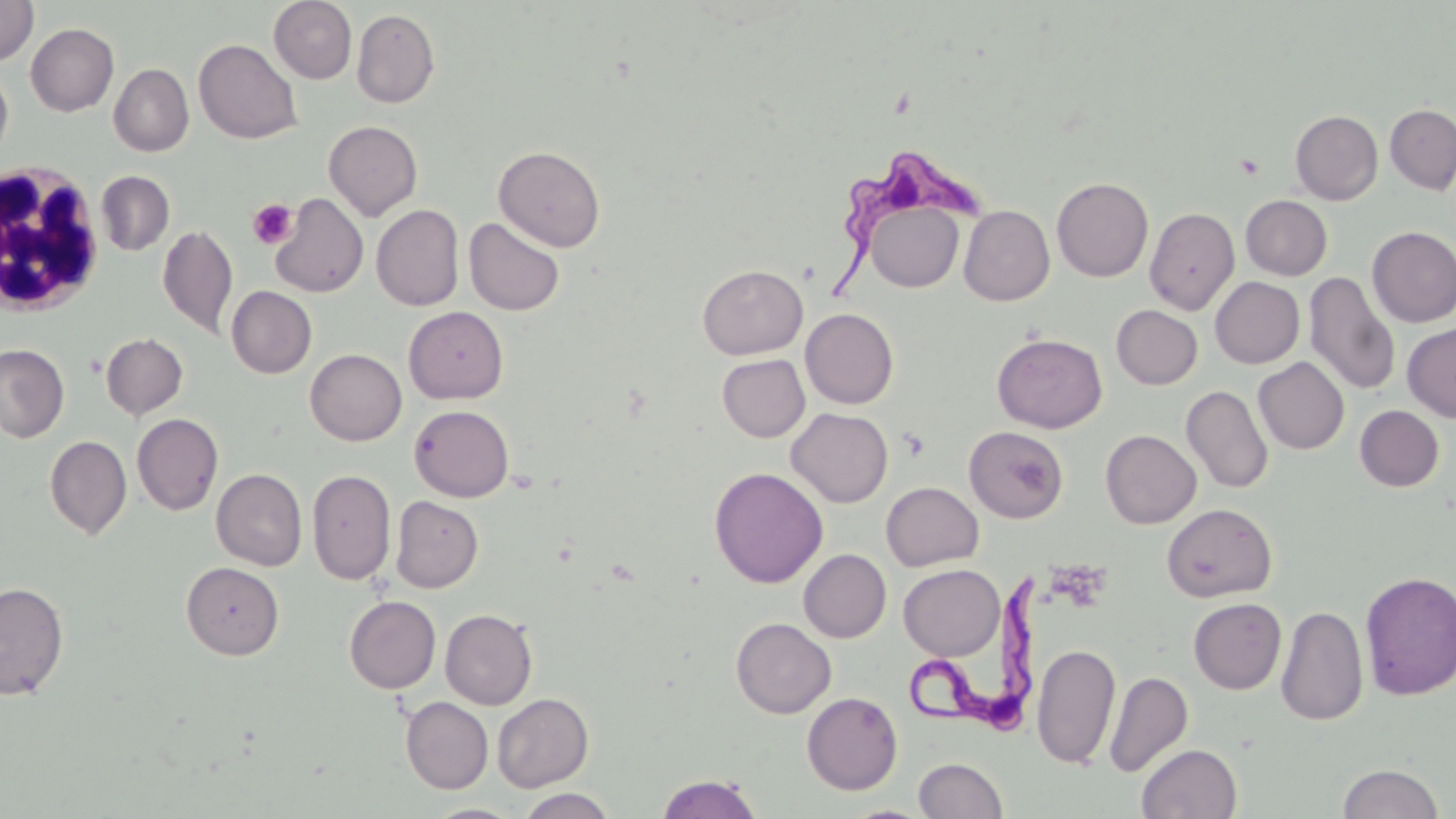
slide-level diagnosis = Trypanosoma brucei
modality = optical microscopy
stain = May-Grünwald-Giemsa
image size = 1456×819 pixels
preparation = thin blood film
Trypanosoma brucei locations = approximate bounding boxes as (x1,y1)-(x2,y2) corner pairs in pixels: (833,147)-(989,290), (903,574)-(1040,731)
uninfected red blood cell locations = approximate bounding boxes as (x1,y1)-(x2,y2) corner pairs in pixels: (0,0)-(38,64), (269,0)-(357,84), (351,8)-(440,108), (26,23)-(118,116), (194,38)-(303,145), (109,63)-(194,156), (0,65)-(13,162), (1385,104)-(1456,194), (1291,110)-(1383,204), (323,120)-(422,220), (493,145)-(606,251), (96,171)-(175,255), (1052,177)-(1153,282), (269,192)-(368,298), (1240,195)-(1332,280), (958,199)-(1153,298), (864,201)-(964,293), (371,204)-(464,311), (959,205)-(1054,306), (1144,207)-(1240,315), (463,217)-(565,316), (157,223)-(237,339), (1367,226)-(1456,327), (698,264)-(807,359), (1304,271)-(1400,395), (1211,276)-(1305,368), (227,286)-(316,378), (1111,304)-(1202,389), (403,306)-(508,404), (800,308)-(898,409), (1403,322)-(1456,423), (101,332)-(188,420), (992,333)-(1107,433), (0,344)-(69,442), (305,348)-(406,445), (717,354)-(810,442), (1253,357)-(1349,454), (1182,385)-(1273,493), (409,404)-(514,502), (1355,405)-(1444,492), (787,408)-(893,507), (132,413)-(223,515), (964,426)-(1069,523), (1100,429)-(1201,528), (45,435)-(132,539), (709,467)-(828,587), (212,468)-(307,570), (307,469)-(395,584), (881,481)-(983,571), (390,496)-(483,593), (1161,503)-(1278,603), (799,549)-(891,642), (181,561)-(284,660), (898,564)-(1004,660), (1359,570)-(1456,700), (0,581)-(69,700), (344,595)-(441,693), (1188,598)-(1287,694), (1276,605)-(1369,726), (440,608)-(537,709), (731,617)-(836,718), (1032,643)-(1121,769), (1105,671)-(1193,778), (802,691)-(903,795), (492,692)-(593,792), (400,697)-(493,793), (1137,744)-(1242,818), (913,757)-(1008,818), (1338,763)-(1445,819), (655,773)-(764,819), (515,788)-(617,818), (422,803)-(523,819)
field of view = single
platelet locations = approximate bounding boxes as (x1,y1)-(x2,y2) corner pairs in pixels: (1235,154)-(1265,180), (248,199)-(298,248), (898,428)-(929,461)
magnification = 1000x
white blood cell locations = approximate bounding boxes as (x1,y1)-(x2,y2) corner pairs in pixels: (1,161)-(107,318)